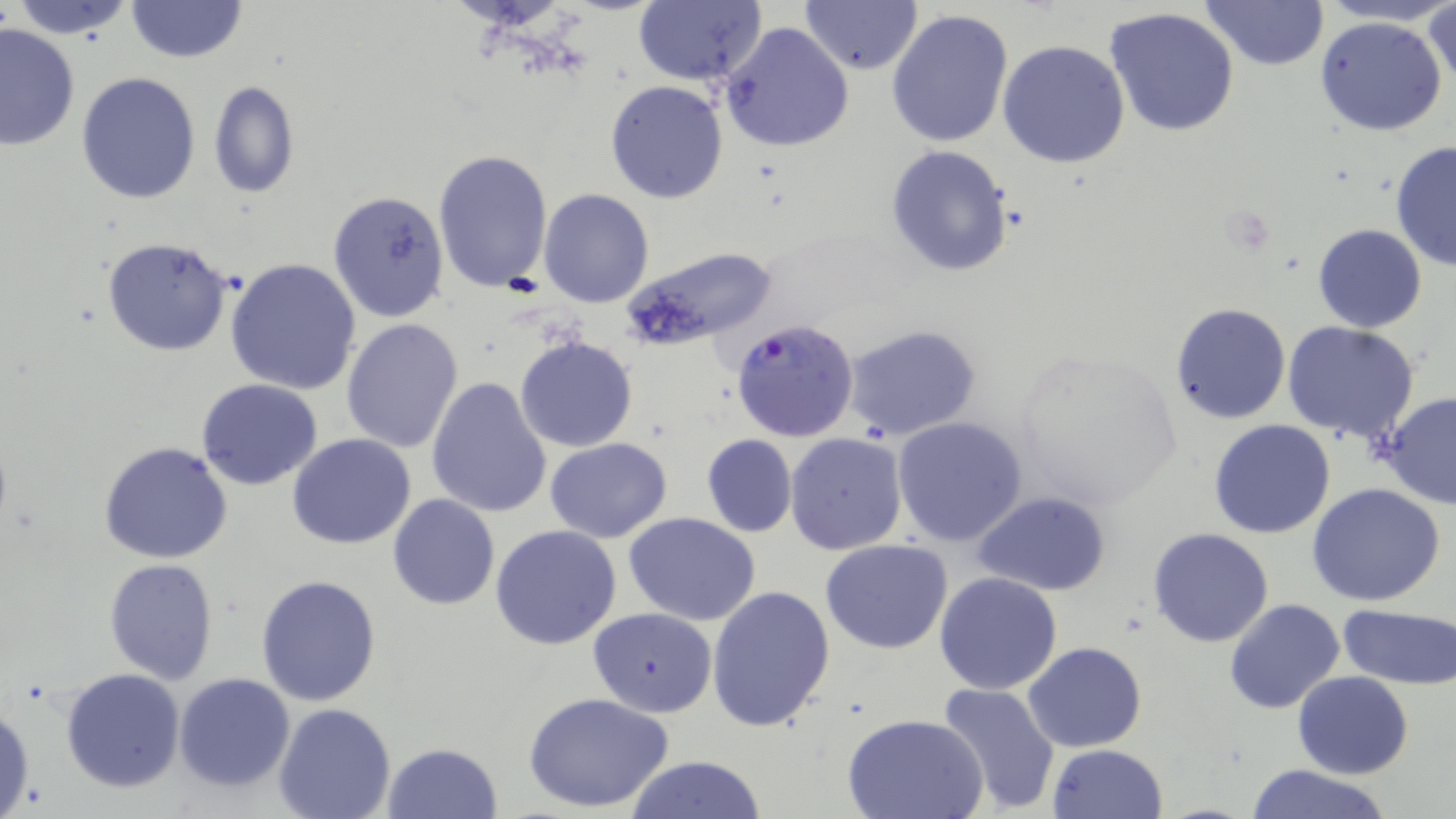

Summary:
  - Coordinate format: approximate bounding boxes as (x1, y1, x2, y2) in pixels
  - Plasmodium falciparum-infected red blood cell locations: (729, 321, 860, 441)
  - Uninfected red blood cell locations: (10, 0, 139, 38), (124, 0, 247, 64), (634, 0, 767, 87), (1203, 0, 1329, 71), (1424, 0, 1456, 93), (801, 1, 923, 75), (1104, 7, 1240, 136), (886, 8, 1015, 149), (1314, 16, 1450, 137), (719, 21, 856, 153), (0, 24, 79, 152), (998, 40, 1130, 169), (77, 73, 201, 206), (206, 80, 299, 198), (605, 81, 728, 203), (1389, 140, 1456, 273), (884, 144, 1014, 277), (433, 149, 554, 293), (538, 188, 655, 307), (327, 191, 450, 323), (1312, 224, 1427, 332), (101, 238, 234, 357), (623, 246, 778, 355), (227, 258, 362, 395), (1169, 302, 1290, 424), (341, 317, 463, 453), (1281, 322, 1423, 443), (843, 323, 984, 442), (513, 333, 638, 453), (1009, 344, 1185, 509), (426, 377, 551, 518), (197, 378, 324, 490), (1380, 393, 1456, 509), (891, 416, 1028, 547), (1207, 420, 1336, 539), (785, 432, 908, 555), (287, 433, 417, 549), (702, 435, 797, 537), (544, 437, 672, 543), (98, 441, 234, 564), (1306, 483, 1447, 606), (973, 491, 1110, 596), (388, 494, 500, 609), (623, 511, 761, 626), (490, 524, 622, 650), (1148, 527, 1274, 647), (821, 540, 952, 654), (103, 559, 219, 685), (934, 571, 1063, 695), (256, 575, 382, 706), (707, 584, 837, 733), (1224, 599, 1345, 713), (1339, 602, 1456, 692), (586, 607, 719, 716), (1024, 641, 1146, 751), (61, 668, 185, 792), (1293, 671, 1412, 778), (174, 673, 296, 791), (932, 680, 1059, 814), (524, 691, 675, 814), (275, 702, 395, 819), (0, 703, 36, 819), (844, 713, 989, 819), (381, 742, 504, 819), (1046, 743, 1166, 819), (627, 755, 768, 817), (1243, 763, 1391, 819)
  - Slide-level diagnosis: Plasmodium falciparum
  - Stain: May-Grünwald-Giemsa
  - Image size: 1456×819 pixels
  - Modality: optical microscopy
  - Preparation: thin blood film
  - Magnification: 1000x
  - Field of view: one of a larger specimen